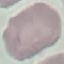

Summary:
  - Result: negative for malaria parasites
  - Stain: Giemsa
  - Preparation: thin blood smear
  - Capture: smartphone camera at the microscope eyepiece
  - Image type: automatically extracted cell patch, resized to 64 × 64 pixels